Locate every Plasmodium parasite.
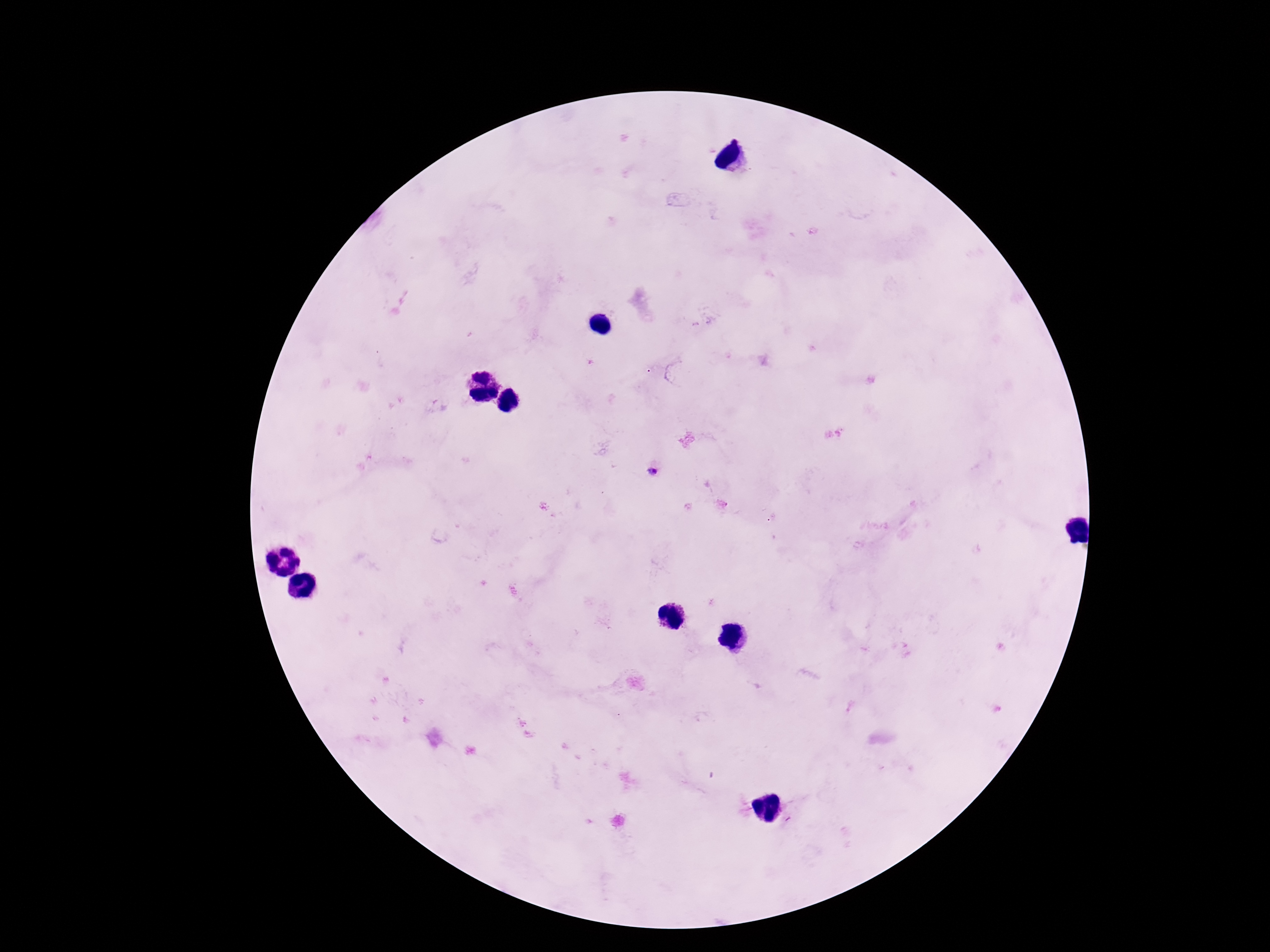

Approximate centers as {x, y} in pixels.
Plasmodium parasites: {652, 472}.

Summary:
  - Magnification: 100x
  - Preparation: thick peripheral-blood smear
  - Image size: 1270×952 pixels
  - Field of view: single
  - Stain: Giemsa
  - Capture: smartphone camera through the microscope eyepiece
  - Patient malaria status: positive